Locate every Plasmodium parasite by life-cycle stage, and every leukocyte.
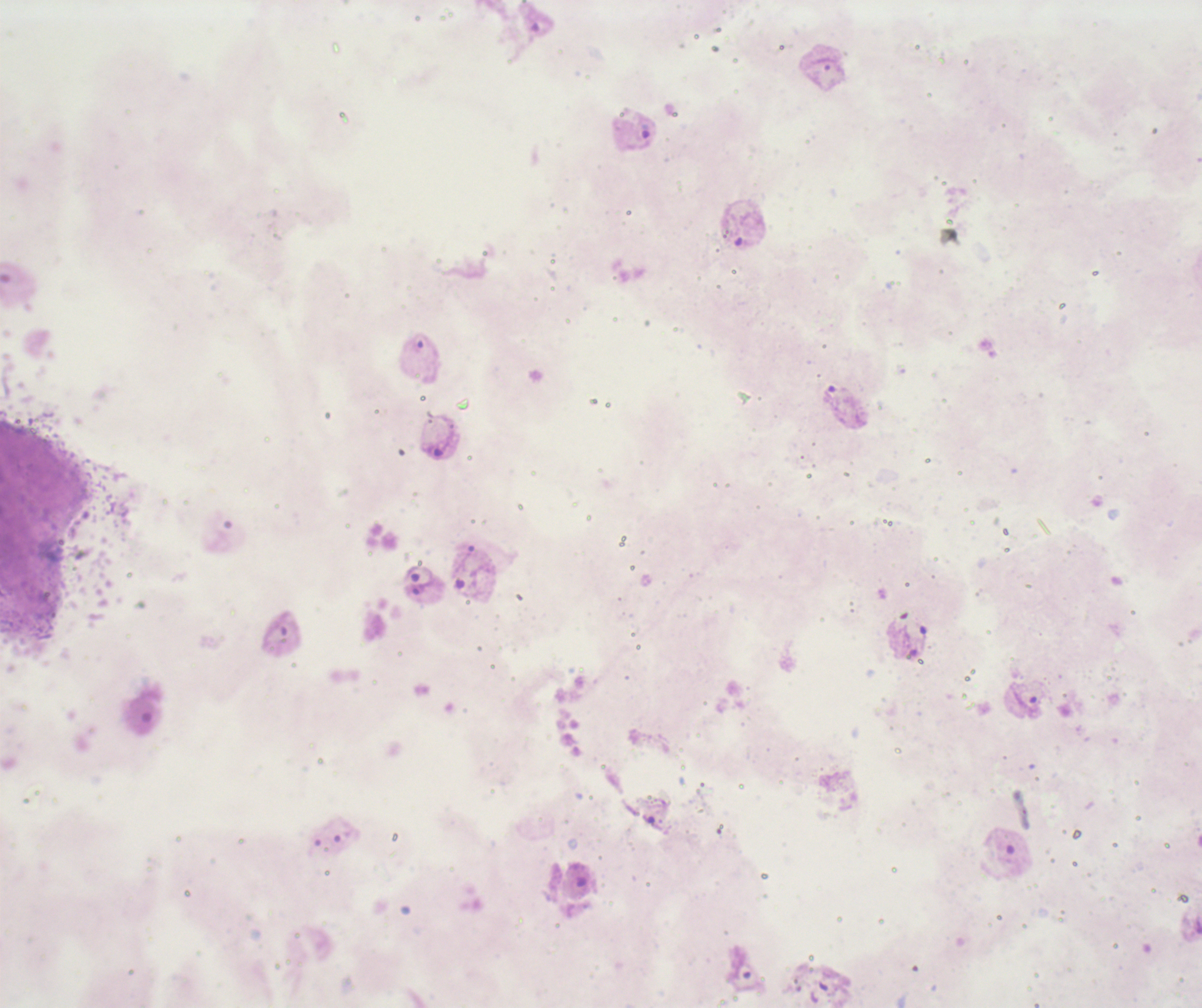
Approximate centers as [x, y] in pixels.
Trophozoites: [640, 132], [439, 439], [418, 581], [1026, 702].
No schizont or gametocyte forms observed.
No leukocytes visible.

Summary:
  - Coloration quality: bad
  - Background quality: unsatisfactory
  - Magnification: 100x
  - Field of view: single
  - Preparation: thick smear of blood
  - Stain: Romanowsky
  - Image size: 1202×1008 pixels
  - Context: previously used in a real diagnosis